Report the malaria status of this cell.
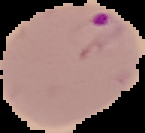

It is parasitized.

Summary:
  - Image type: segmented cell region with the area outside set to black
  - Preparation: thin blood film
  - Image size: 145×133 pixels